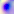

identification = Toxoplasma gondii
modality = photomicrograph
magnification = 400x